State which parasite is depicted.
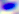
Toxoplasma gondii.

Micrograph. 400x magnification.